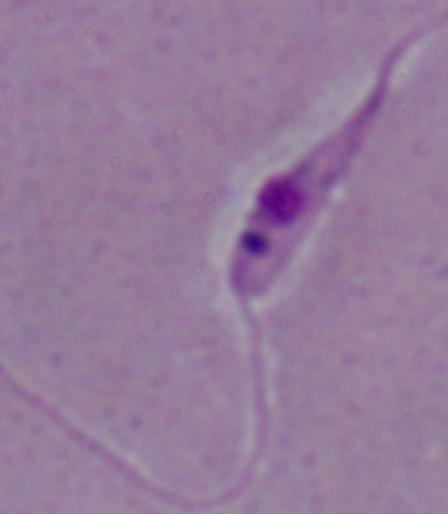
magnification = 1000x
identification = Leishmania
modality = photomicrograph